State which cell type is depicted.
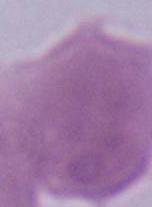

This is an erythrocyte.

Micrograph. Captured at 1000x magnification.